Assess the morphology of the red blood cells.
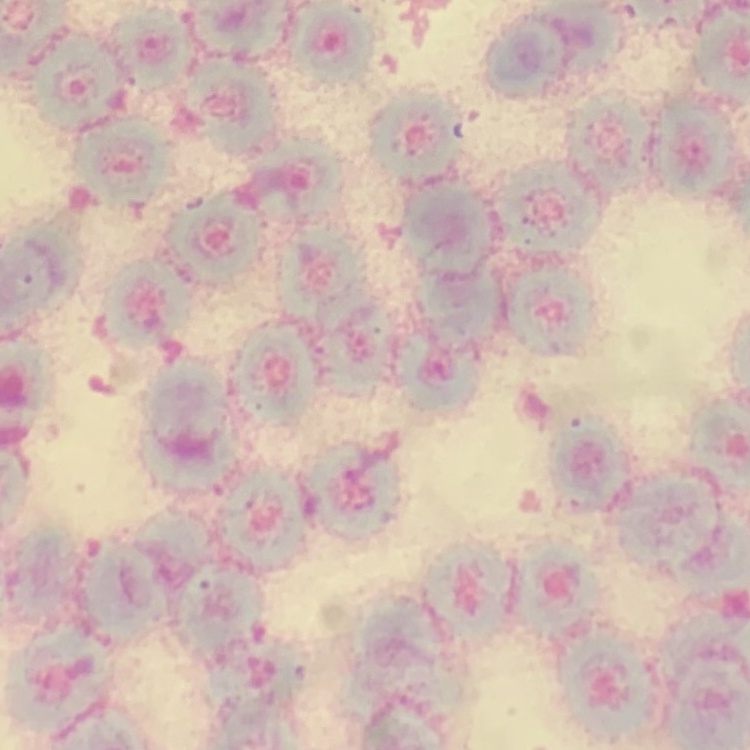
Rouleaux formation.

Square crop of a larger photomicrograph. Thin peripheral smear. Field's or Giemsa stain.